Report the malaria status of this cell.
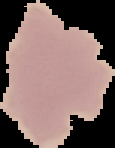
It is uninfected.

Cell region segmented out of the field of view; the surrounding area is masked to black. From a thin blood smear. Image is 115×148 pixels.